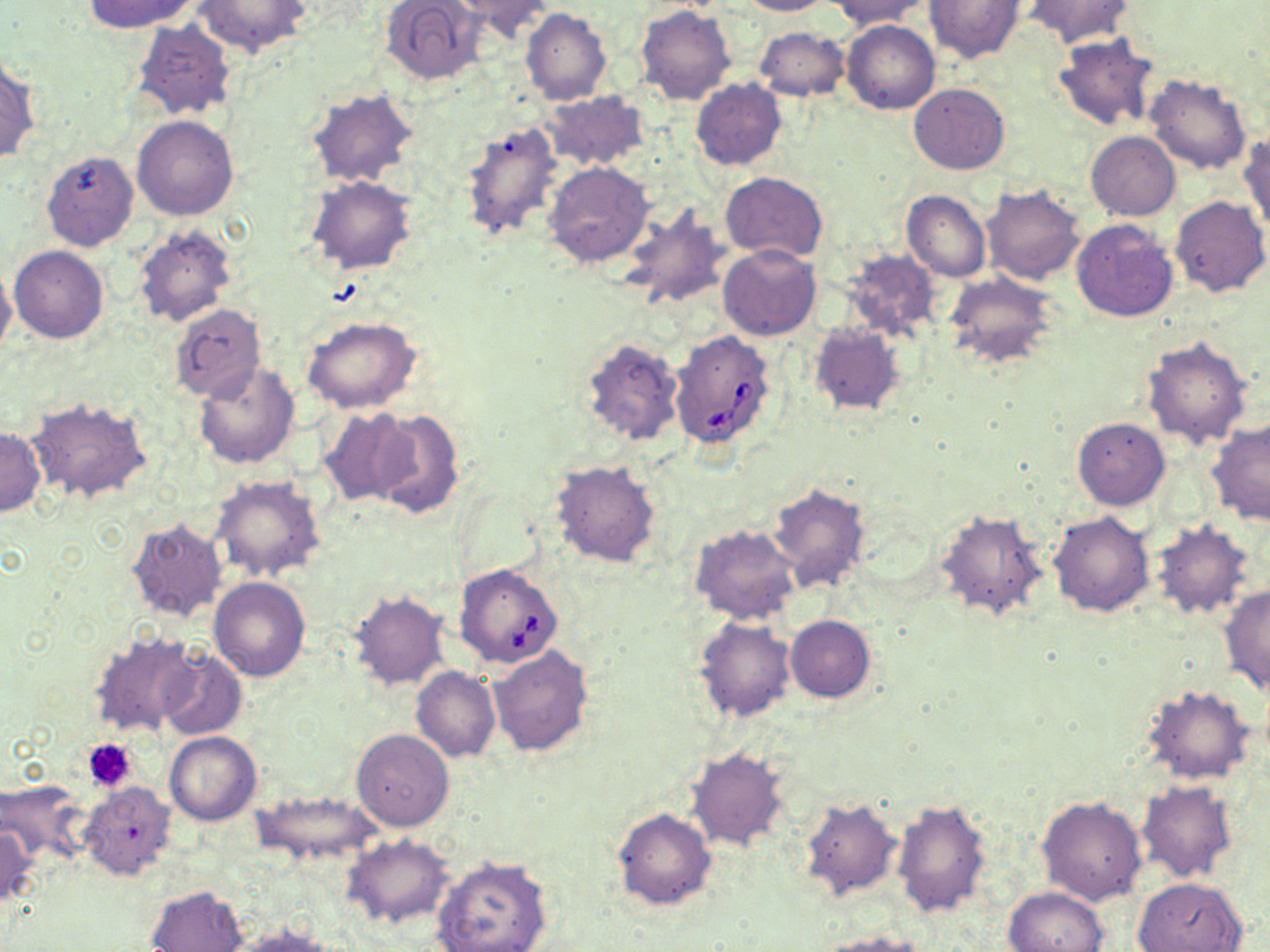
Approximate bounding boxes as (x1,y1)-(x2,y2) corner pairs in pixels. Platelet locations: (83,737)-(136,792). Babesia divergens-infected red blood cell locations: (669,329)-(776,448), (453,562)-(563,669). Uninfected red blood cell locations: (85,0)-(196,33), (196,0)-(312,57), (380,0)-(485,84), (458,0)-(556,42), (735,0)-(833,16), (829,0)-(929,29), (924,1)-(1023,62), (1025,1)-(1133,47), (635,5)-(737,106), (520,8)-(611,105), (131,19)-(236,122), (843,20)-(939,114), (754,27)-(851,100), (1053,33)-(1159,131), (0,56)-(40,165), (1145,74)-(1251,175), (690,79)-(786,169), (911,83)-(1008,175), (307,87)-(417,188), (542,90)-(650,171), (132,115)-(239,220), (459,119)-(566,243), (1086,131)-(1179,221), (1239,132)-(1270,232), (42,150)-(138,252), (543,162)-(653,269), (719,172)-(826,262), (306,176)-(416,274), (980,184)-(1086,285), (902,190)-(990,282), (1170,196)-(1269,297), (618,208)-(730,312), (1071,219)-(1179,322), (132,225)-(237,329), (719,243)-(821,341), (9,245)-(107,343), (839,249)-(942,345), (0,265)-(16,356), (947,274)-(1058,369), (169,305)-(266,403), (301,316)-(423,414), (808,323)-(904,417), (580,336)-(683,448), (1141,336)-(1252,447), (193,362)-(301,470), (24,397)-(151,503), (319,406)-(418,505), (369,408)-(464,520), (1072,418)-(1169,510), (1207,420)-(1270,526), (0,425)-(44,517), (550,459)-(662,568), (212,476)-(326,583), (768,482)-(869,591), (452,489)-(544,580), (932,508)-(1049,623), (1048,511)-(1155,618), (125,518)-(228,624), (1149,521)-(1254,620), (690,524)-(802,626), (209,576)-(311,682), (1219,586)-(1270,695), (349,590)-(450,691), (786,615)-(875,702), (694,617)-(797,721), (88,629)-(202,738), (487,645)-(594,756), (156,649)-(246,740), (411,667)-(499,762), (1140,684)-(1256,786), (352,729)-(455,832), (164,731)-(262,826), (686,746)-(791,852), (0,780)-(90,865), (1137,780)-(1237,882), (79,782)-(178,882), (250,790)-(386,866), (797,796)-(903,903), (1036,796)-(1147,905), (892,798)-(991,917), (613,808)-(716,911), (0,821)-(39,913), (343,835)-(455,930), (433,855)-(552,952), (1134,877)-(1247,952), (146,885)-(248,951), (1002,886)-(1110,952), (223,928)-(336,952), (807,933)-(927,952). Slide-level diagnosis: Babesia divergens. Light microscopy. Captured at 1000x magnification. Thin blood film. Single field of view. May-Grünwald-Giemsa stain. Image is 1270×952 pixels.